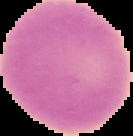

{
  "image_size": "133×136 pixels",
  "preparation": "thin blood smear",
  "image_type": "segmented cell region on a black background",
  "result": "negative for Plasmodium parasites"
}